Give the extent of all Plasmodium ovale-infected red blood cells.
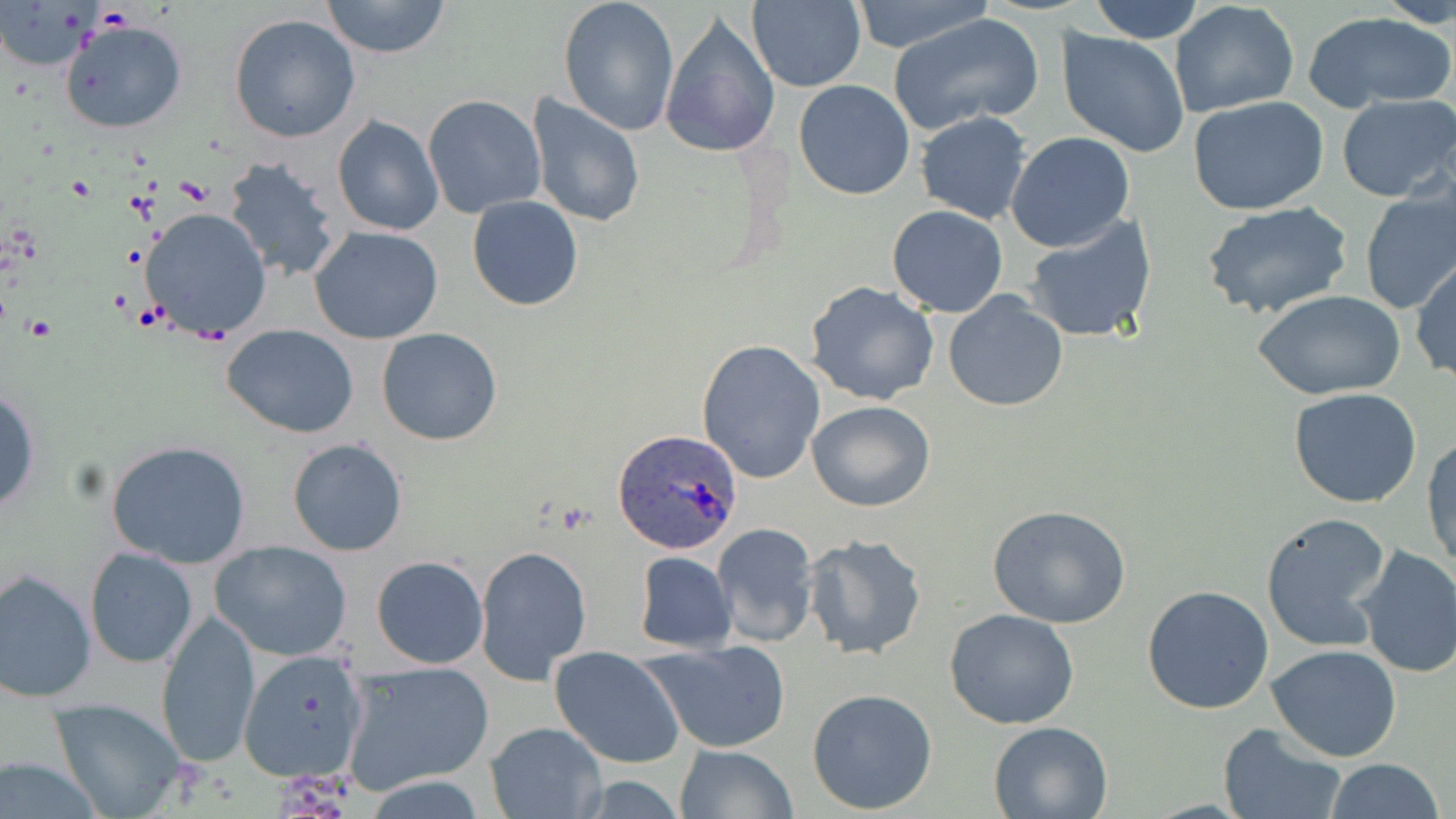

Approximate bounding boxes as (x1,y1)-(x2,y2) corner pairs in pixels.
Plasmodium ovale-infected red blood cells: (613,431)-(742,555).

Summary:
  - Uninfected red blood cell locations: (321,0)-(452,60), (557,0)-(681,137), (746,0)-(865,91), (849,0)-(996,54), (1087,0)-(1206,43), (1380,0)-(1456,29), (1169,2)-(1300,119), (1304,9)-(1455,113), (888,11)-(1045,137), (227,13)-(361,143), (659,14)-(782,160), (59,19)-(188,134), (1055,29)-(1190,160), (793,80)-(917,200), (1335,93)-(1455,204), (421,94)-(546,219), (526,94)-(646,228), (1188,96)-(1329,215), (915,110)-(1031,225), (332,115)-(446,237), (1005,131)-(1136,252), (222,155)-(343,284), (1358,189)-(1456,315), (467,196)-(584,311), (1200,200)-(1352,319), (887,203)-(1008,318), (140,207)-(271,343), (1023,215)-(1157,344), (308,226)-(445,344), (1411,257)-(1455,384), (804,281)-(942,406), (942,290)-(1068,413), (1253,291)-(1403,400), (222,324)-(361,437), (376,328)-(503,446), (696,338)-(825,484), (0,388)-(41,515), (1288,388)-(1423,509), (806,400)-(935,512), (1423,432)-(1455,571), (286,438)-(408,556), (104,440)-(252,569), (986,505)-(1134,629), (1259,511)-(1394,653), (712,522)-(820,648), (802,533)-(928,661), (210,539)-(352,662), (1353,544)-(1456,679), (476,547)-(594,686), (84,548)-(197,669), (633,551)-(738,653), (371,555)-(489,669), (1,566)-(96,702), (1142,586)-(1275,715), (155,609)-(261,768), (942,609)-(1081,730), (641,639)-(793,754), (1266,644)-(1402,761), (238,646)-(371,785), (550,647)-(686,769), (340,659)-(496,796), (806,687)-(938,814), (47,698)-(188,818), (987,719)-(1115,817), (483,721)-(608,819), (1217,723)-(1348,819), (674,744)-(799,819), (1,752)-(108,818), (1324,758)-(1444,819)
  - Slide-level diagnosis: Plasmodium ovale
  - Stain: May-Grünwald-Giemsa
  - Magnification: 1000x
  - Preparation: thin blood smear
  - Modality: optical microscopy
  - Field of view: one of a larger specimen
  - Image size: 1456×819 pixels